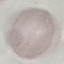

Malaria status: uninfected. Giemsa-stained preparation. Cell patch, automatically extracted from a larger field of view and resized to 64 × 64 pixels. Photographed with a smartphone camera at the microscope eyepiece. Thin smear of blood.